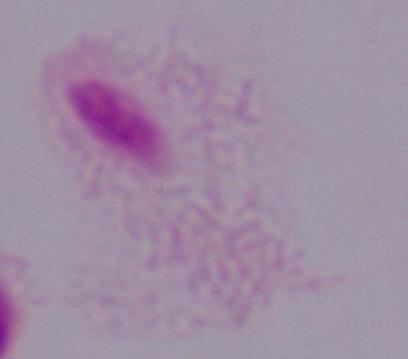 A trichomonad is shown. Photomicrograph. Captured at 1000x magnification.